Identify the parasite.
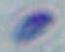

Toxoplasma gondii.

modality = micrograph
magnification = 1000x